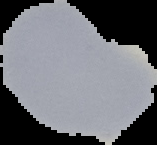
Image is 157×145 pixels. Result: no malaria parasites seen. Cell region segmented out of the field of view; the surrounding area is masked to black. From a thin blood smear.